Locate every uninfected red blood cell.
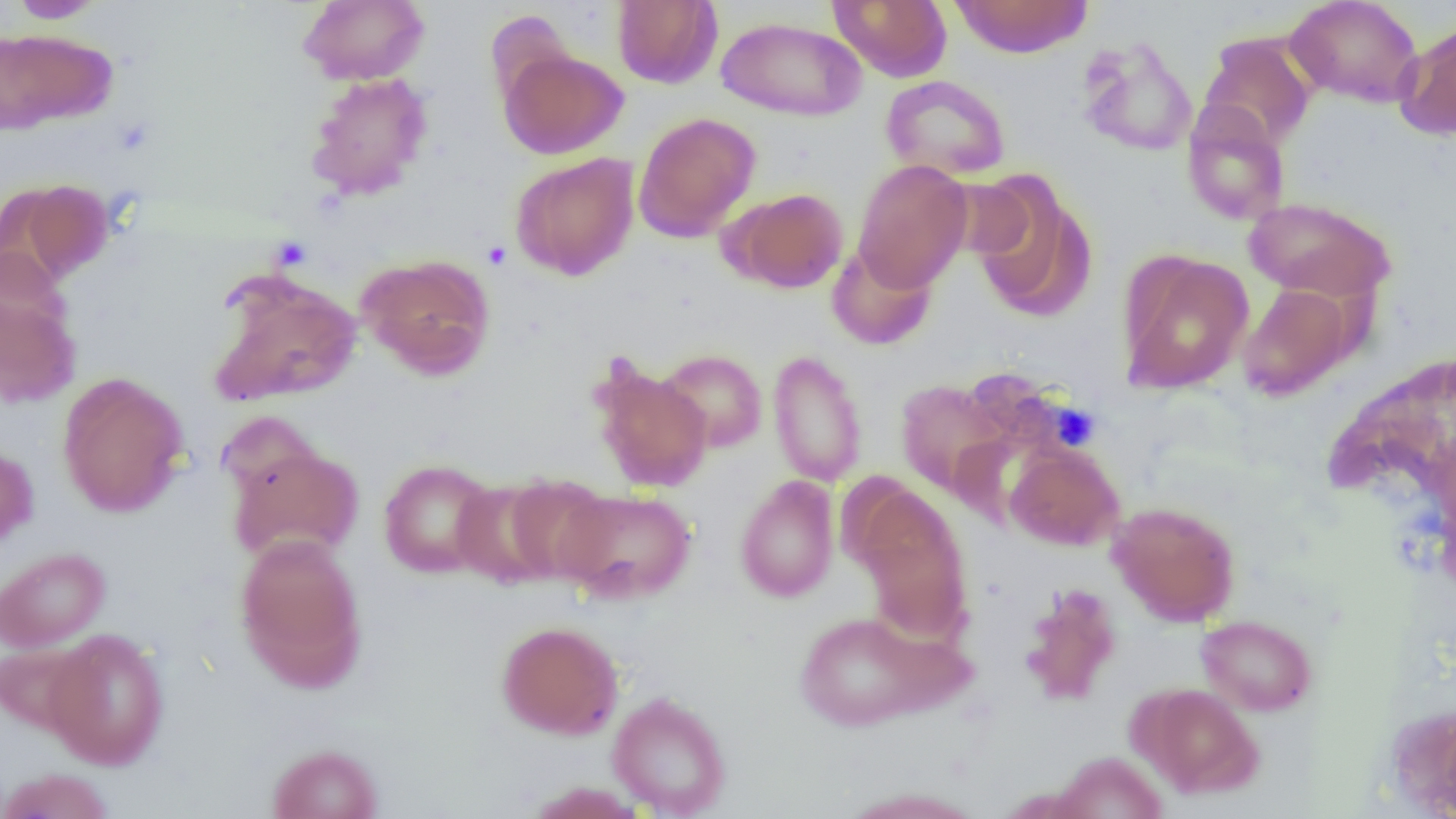

Approximate bounding boxes as [x1, y1, x2, y2] in pixels.
Uninfected red blood cells: [8, 0, 107, 23], [297, 0, 430, 86], [828, 0, 952, 83], [950, 0, 1093, 58], [1285, 0, 1424, 108], [611, 1, 723, 89], [715, 16, 867, 121], [1396, 20, 1456, 141], [0, 28, 116, 131], [1199, 33, 1316, 149], [1078, 37, 1199, 157], [497, 47, 629, 159], [305, 72, 433, 201], [880, 75, 1011, 181], [1181, 102, 1291, 226], [633, 111, 761, 242], [509, 152, 640, 281], [853, 158, 973, 292], [966, 174, 1096, 322], [3, 178, 115, 288], [728, 188, 848, 293], [1243, 196, 1397, 302], [825, 242, 938, 351], [1116, 249, 1253, 394], [356, 253, 496, 379], [206, 268, 363, 409], [0, 282, 80, 409], [1238, 284, 1355, 402], [656, 348, 769, 454], [767, 349, 868, 487], [588, 359, 713, 493], [57, 371, 189, 518], [894, 378, 1010, 497], [215, 410, 324, 507], [0, 444, 38, 555], [228, 444, 364, 564], [1004, 444, 1125, 550], [378, 459, 499, 579], [500, 473, 614, 585], [734, 475, 840, 603], [450, 478, 564, 589], [852, 485, 973, 639], [556, 488, 697, 603], [1107, 500, 1241, 625], [234, 534, 367, 690], [0, 546, 110, 652], [1019, 583, 1122, 706], [794, 611, 942, 731], [1196, 614, 1317, 716], [495, 621, 624, 740], [43, 628, 170, 769], [0, 643, 97, 736], [1134, 683, 1265, 799], [607, 691, 732, 817], [266, 743, 383, 819], [1051, 751, 1168, 819], [0, 768, 115, 819], [524, 781, 650, 819], [834, 786, 989, 819].

Platelet locations: [482, 240, 512, 270], [1049, 402, 1100, 451]. Slide-level diagnosis: no evidence of blood parasites. Optical microscopy. Image is 1456×819 pixels. Thin blood film. 1000x magnification. One field of a larger specimen.